Comment on the morphology of the red blood cells.
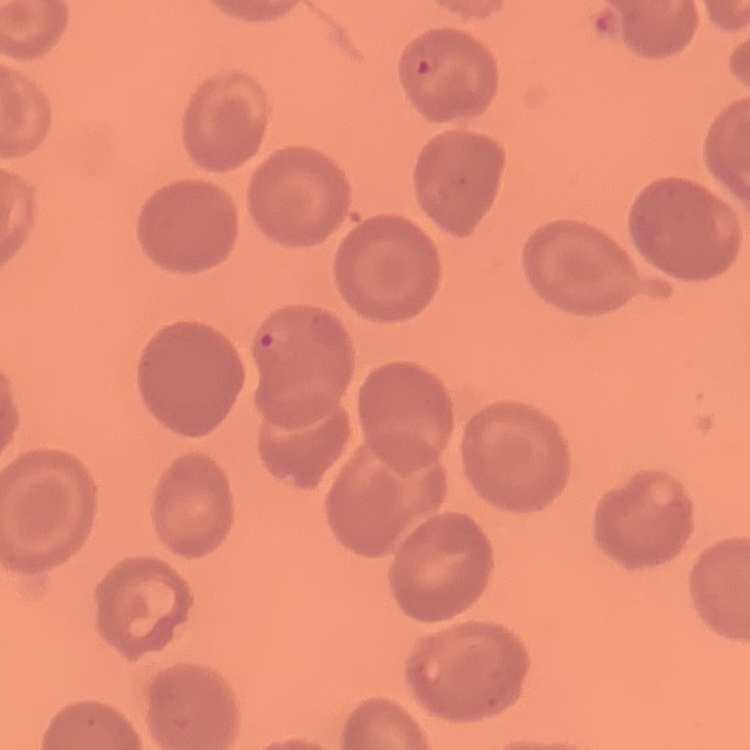

They show no rouleaux formation.

Square crop of a larger photomicrograph. Field's or Giemsa stain. Thin blood smear.